Comment on the morphology of the red blood cells.
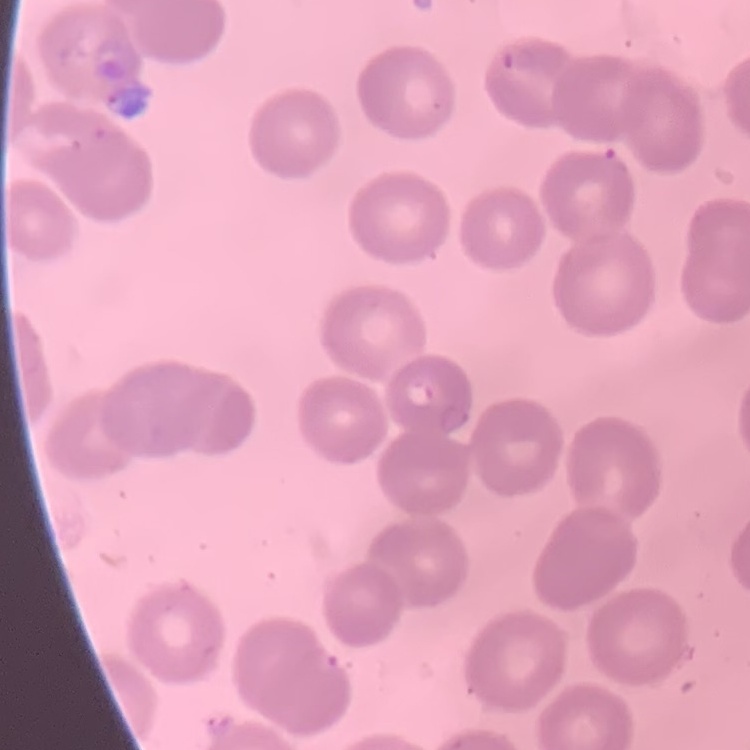

No rouleaux formation.

Summary:
  - Stain: Field's or Giemsa
  - Preparation: thin peripheral smear
  - Image type: one tile cut from a larger photomicrograph